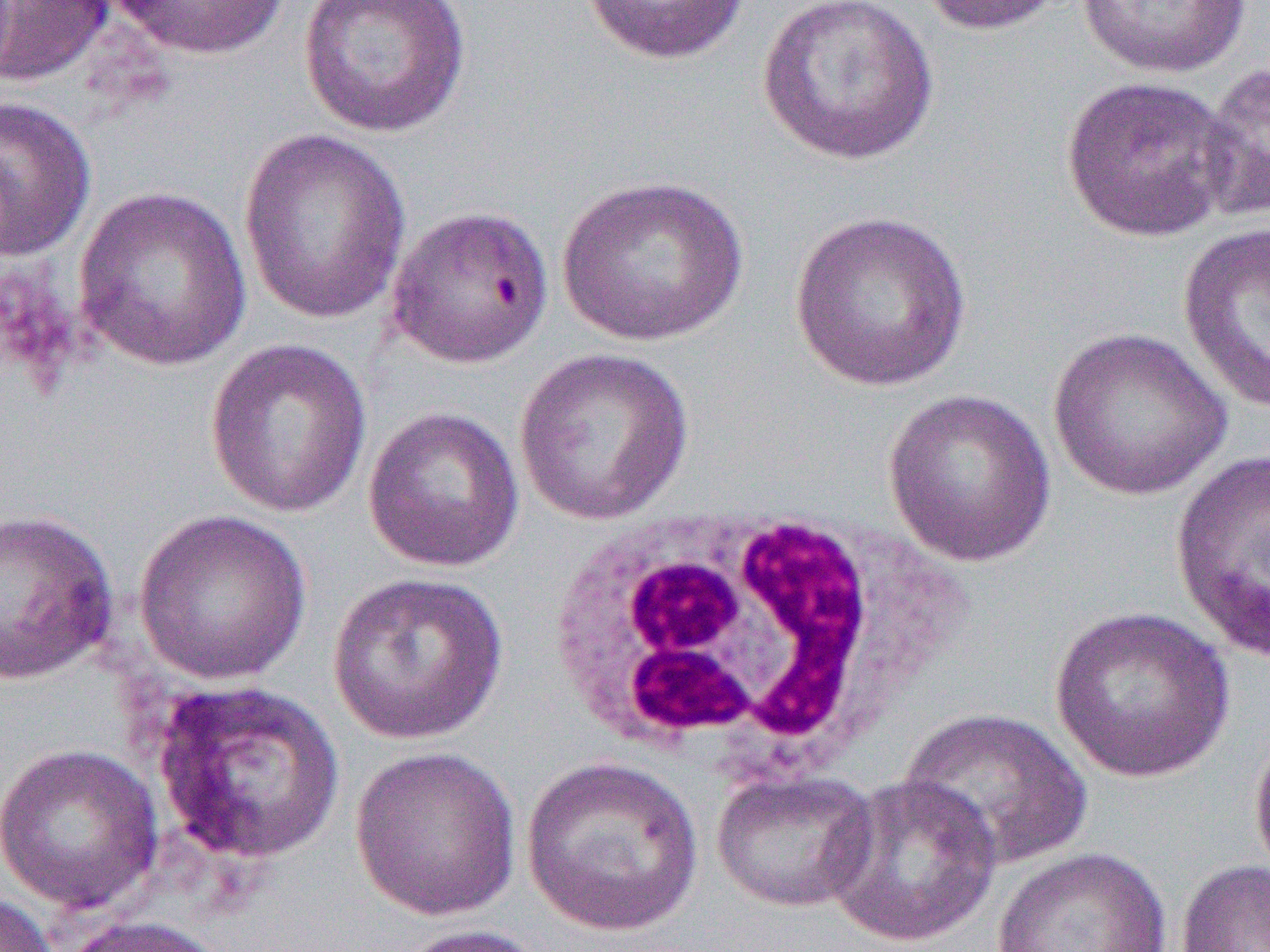
{
  "slide_level_diagnosis": "Plasmodium falciparum",
  "preparation": "thin blood film",
  "white_blood_cell_locations": "approximate bounding boxes as named x1/y1/x2/y2 corners in pixels: (x1=558, y1=504, x2=886, y2=779)",
  "magnification": "1000x",
  "modality": "optical microscopy",
  "image_size": "1270×952 pixels",
  "field_of_view": "single",
  "uninfected_red_blood_cell_locations": "approximate bounding boxes as named x1/y1/x2/y2 corners in pixels: (x1=1, y1=0, x2=114, y2=88), (x1=107, y1=0, x2=292, y2=61), (x1=297, y1=0, x2=473, y2=139), (x1=578, y1=0, x2=752, y2=67), (x1=755, y1=0, x2=941, y2=168), (x1=913, y1=0, x2=1073, y2=36), (x1=1076, y1=1, x2=1253, y2=79), (x1=1198, y1=60, x2=1270, y2=223), (x1=1059, y1=73, x2=1241, y2=243), (x1=0, y1=96, x2=97, y2=262), (x1=237, y1=128, x2=412, y2=325), (x1=557, y1=174, x2=751, y2=347), (x1=73, y1=185, x2=252, y2=372), (x1=385, y1=205, x2=555, y2=368), (x1=787, y1=208, x2=973, y2=392), (x1=1176, y1=220, x2=1270, y2=414), (x1=1046, y1=327, x2=1233, y2=501), (x1=204, y1=337, x2=373, y2=519), (x1=513, y1=346, x2=695, y2=526), (x1=882, y1=388, x2=1057, y2=568), (x1=362, y1=406, x2=525, y2=573), (x1=1170, y1=447, x2=1270, y2=662), (x1=0, y1=508, x2=120, y2=685), (x1=133, y1=508, x2=313, y2=686), (x1=327, y1=571, x2=509, y2=746), (x1=1048, y1=605, x2=1235, y2=783), (x1=147, y1=679, x2=347, y2=867), (x1=898, y1=707, x2=1094, y2=870), (x1=1249, y1=725, x2=1270, y2=882), (x1=0, y1=742, x2=164, y2=915), (x1=349, y1=745, x2=523, y2=921), (x1=520, y1=756, x2=704, y2=937), (x1=711, y1=768, x2=880, y2=913), (x1=823, y1=774, x2=1002, y2=950), (x1=993, y1=846, x2=1172, y2=952), (x1=1175, y1=859, x2=1270, y2=952), (x1=0, y1=890, x2=59, y2=952), (x1=58, y1=915, x2=229, y2=952), (x1=389, y1=923, x2=555, y2=952)"
}